Classify this cell by malaria status.
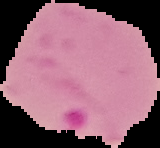
It is parasitized.

Image is 160×148 pixels. From a thin blood film. Segmented cell region on a black background.